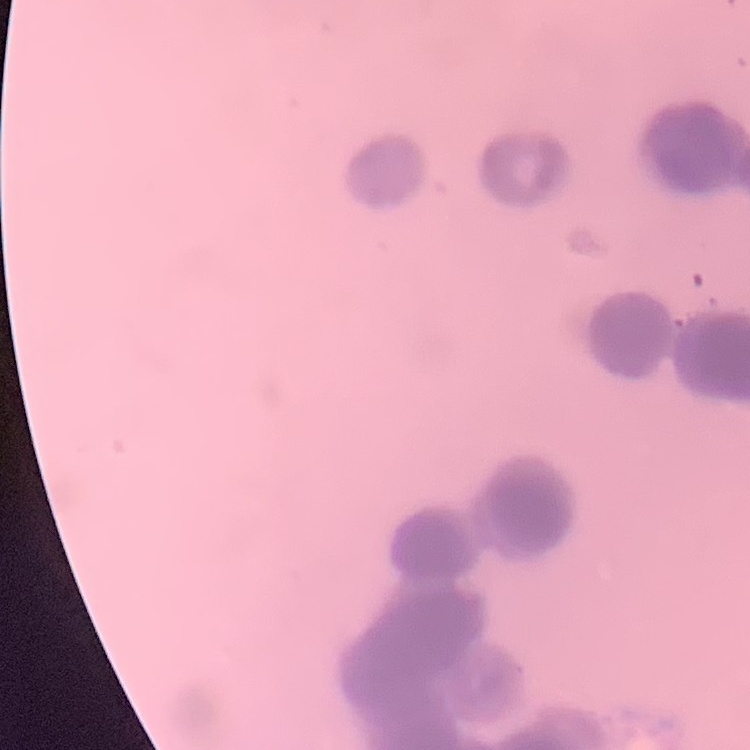
The red blood cells exhibit rouleaux formation. Thin blood film. One tile cut from a larger photomicrograph. Field's or Giemsa stain.